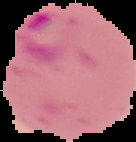 From a thin blood smear. Image is 136×142 pixels. Cell region segmented out of the field of view; the surrounding area is masked to black. Malaria status: parasitized.